Assess this cell for malaria.
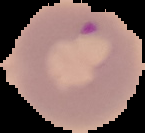

It is parasitized.

Summary:
  - Image size: 145×133 pixels
  - Preparation: thin blood film
  - Image type: segmented cell region with the area outside set to black